Classify this cell by malaria status.
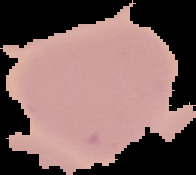
Uninfected.

Segmented cell region on a black background. From a thin blood smear. Image is 196×175 pixels.